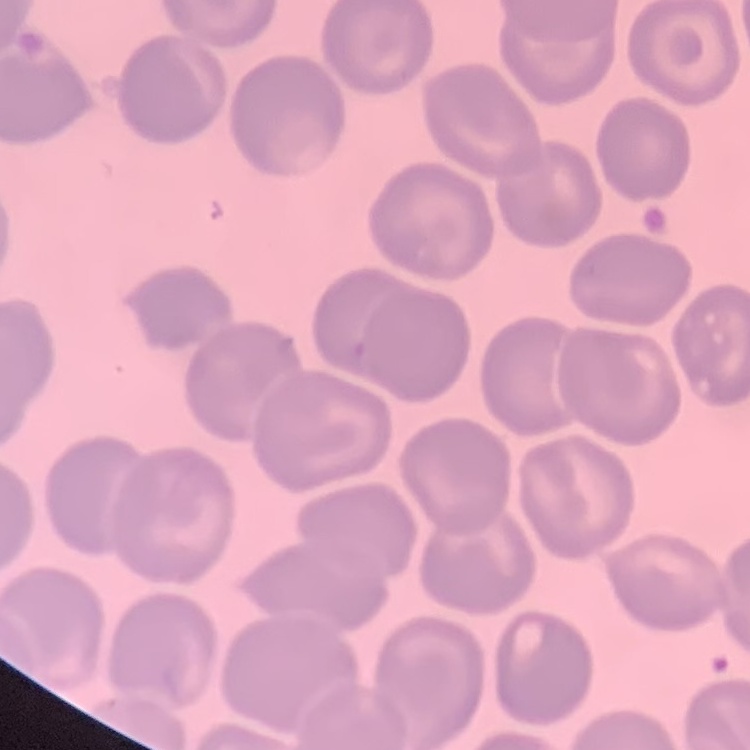
Summary:
  - Red blood cell morphology: no rouleaux formation
  - Stain: Field's or Giemsa
  - Image type: one tile cut from a larger photomicrograph
  - Preparation: thin blood film